Describe the morphology of the red blood cells.
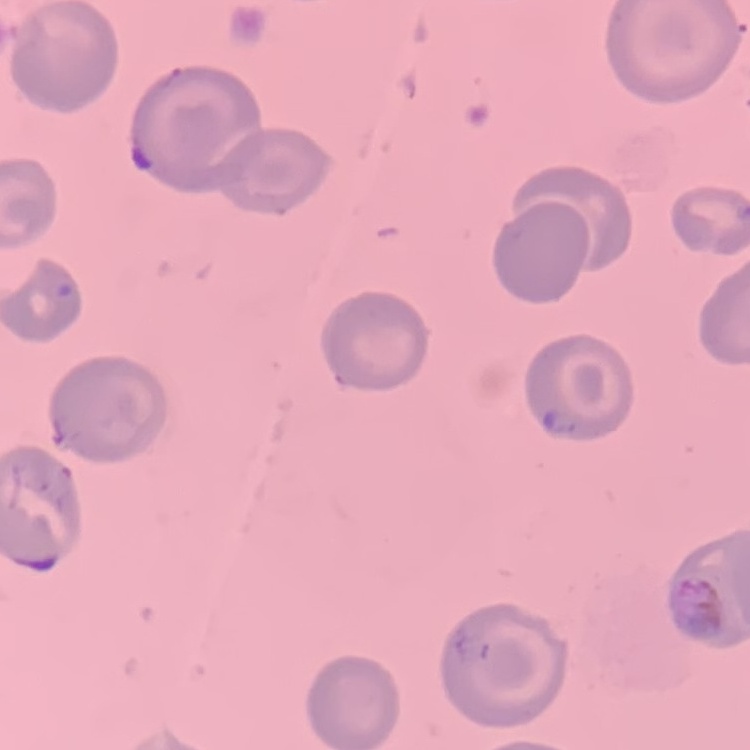
No rouleaux formation.

Square crop of a larger photomicrograph. Thin peripheral smear. Stained with either Field's or Giemsa.